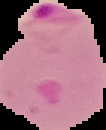 Cell region segmented out of the field of view; the surrounding area is masked to black. Image is 106×130 pixels. From a thin blood film. Malaria status: parasitized.